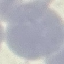

result = no malaria parasites detected
image type = automatically extracted cell patch, resized to 64 × 64 pixels
preparation = thin blood smear
stain = Giemsa
capture = smartphone through the microscope eyepiece